Report the malaria status of this cell.
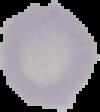
Uninfected.

From a thin blood film. Image is 100×112 pixels. The area outside the segmented cell region is set to black.